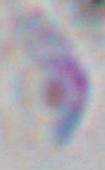
modality: photomicrograph
identification: Toxoplasma gondii
magnification: 1000x